Report the malaria status of this cell.
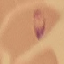
It is parasitized.

Photographed with a smartphone camera at the microscope eyepiece. Cell patch, automatically extracted from a larger field of view and resized to 64 × 64 pixels. Thin smear of blood. Giemsa-stained preparation.